Report the malaria status of this cell.
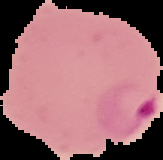

It is parasitized.

preparation = thin blood film
image size = 163×160 pixels
image type = segmented cell region on a black background